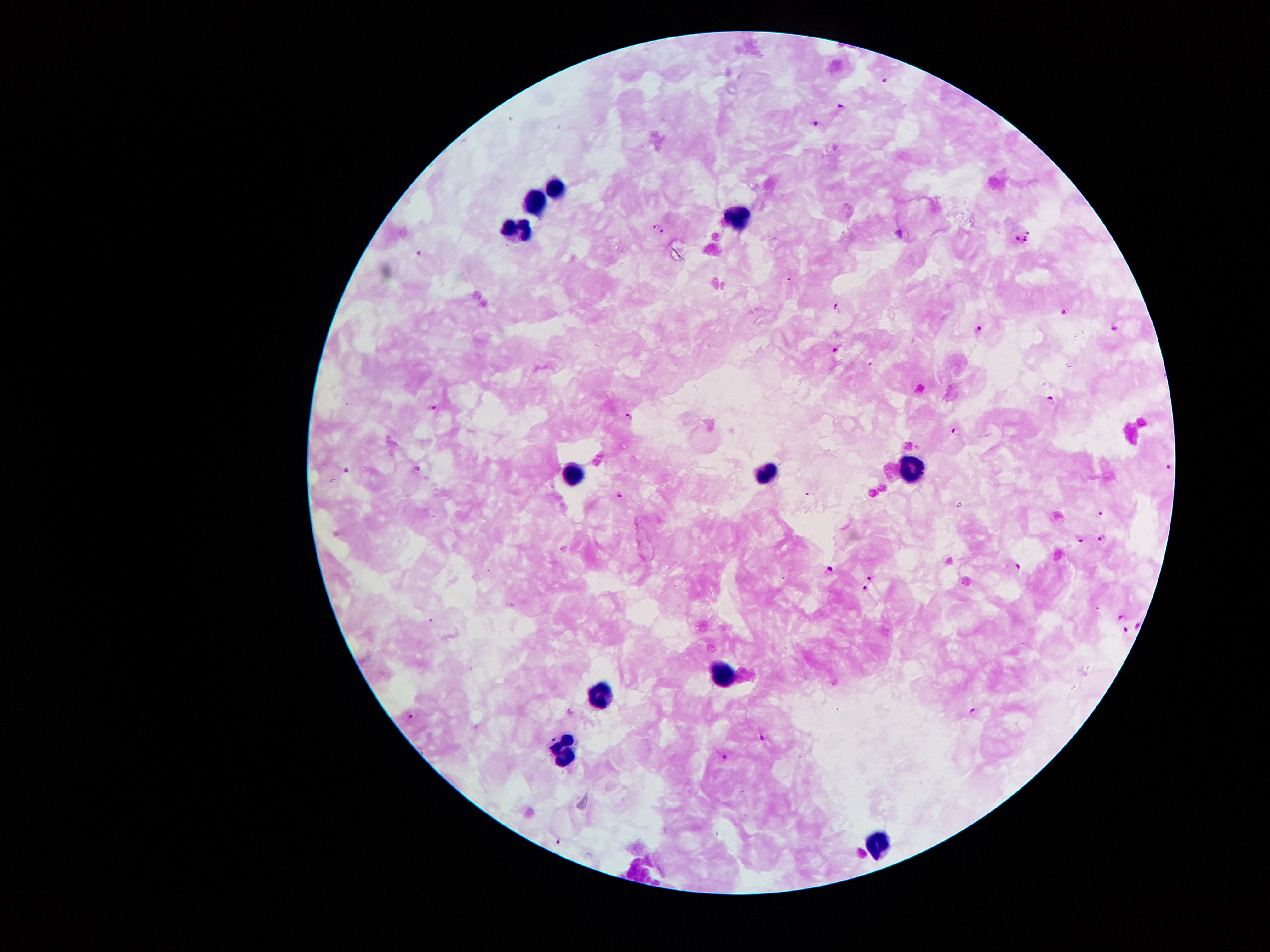

Approximate centers as {x, y} in pixels.
Summary:
  - Plasmodium parasite locations: {885, 80}, {842, 105}, {815, 124}, {653, 225}, {663, 232}, {1030, 232}, {1018, 240}, {1025, 240}, {419, 253}, {837, 306}, {1065, 311}, {980, 328}, {1115, 329}, {835, 349}, {1052, 399}, {432, 407}, {628, 417}, {957, 432}, {1168, 465}, {346, 468}, {417, 468}, {620, 495}, {1102, 513}, {1101, 538}, {1081, 541}, {1019, 567}, {830, 569}, {870, 578}, {865, 587}, {1121, 617}, {1137, 624}, {1126, 629}, {973, 713}, {411, 715}, {554, 737}, {763, 737}, {724, 755}, {558, 840}
  - Leukocyte locations: {549, 186}, {533, 197}, {735, 218}, {515, 226}, {766, 471}, {908, 473}, {574, 475}, {724, 673}, {598, 694}, {561, 752}, {877, 840}
  - Patient malaria status: infected with Plasmodium falciparum
  - Field of view: single
  - Magnification: 100x
  - Capture: smartphone camera through the microscope eyepiece
  - Preparation: thick blood smear
  - Image size: 1270×952 pixels
  - Stain: Giemsa